Outline each blood parasite and name the species.
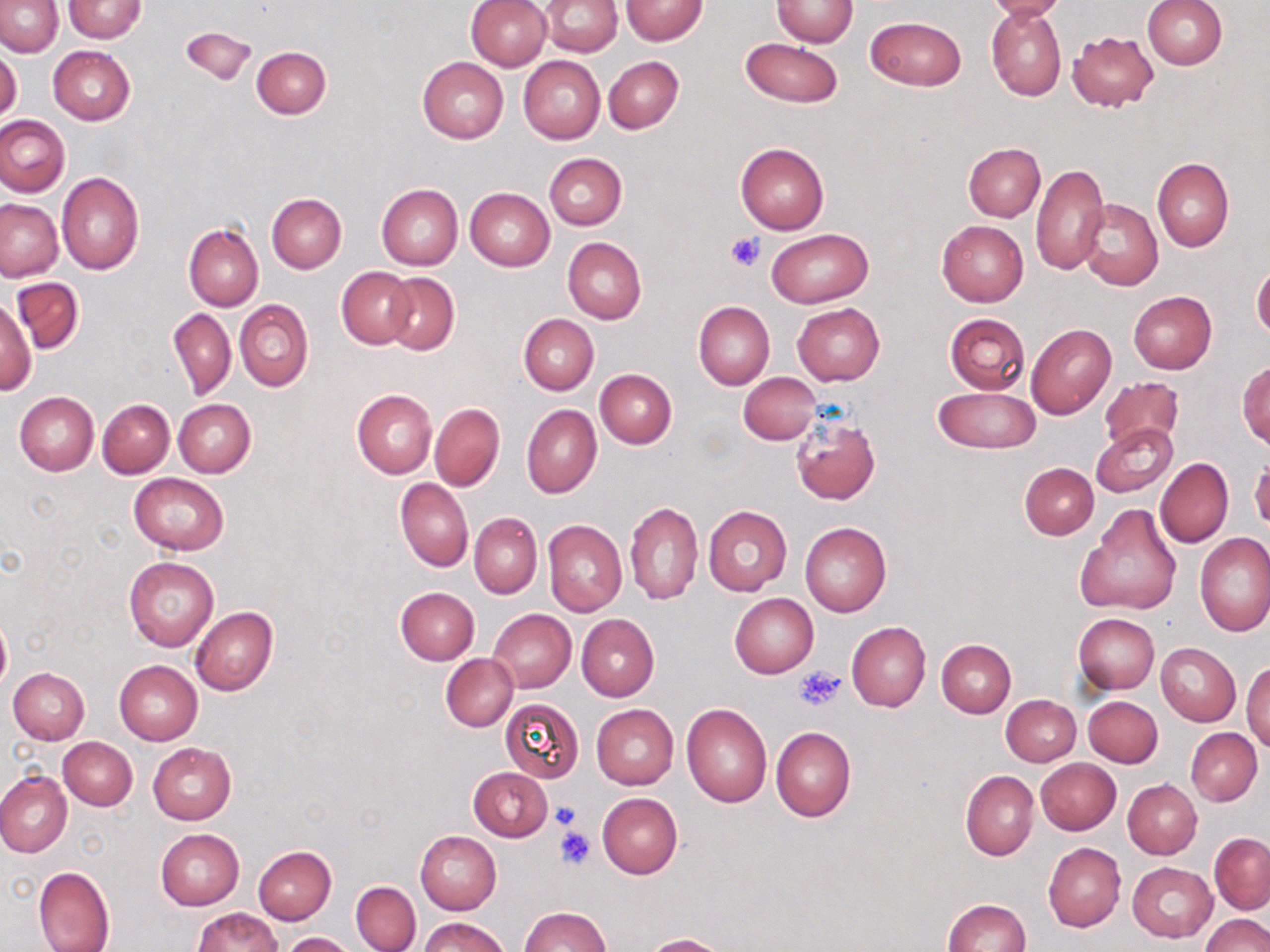
No blood parasites seen.

Summary:
  - Coordinate format: approximate bounding boxes as named x1/y1/x2/y2 corners in pixels
  - Platelet locations: (x1=726, y1=232, x2=766, y2=271), (x1=795, y1=666, x2=846, y2=711), (x1=552, y1=802, x2=582, y2=829), (x1=554, y1=825, x2=596, y2=869)
  - Uninfected red blood cell locations: (x1=0, y1=0, x2=64, y2=56), (x1=63, y1=0, x2=146, y2=43), (x1=540, y1=0, x2=622, y2=56), (x1=620, y1=0, x2=707, y2=45), (x1=771, y1=0, x2=858, y2=47), (x1=982, y1=0, x2=1067, y2=22), (x1=1142, y1=0, x2=1227, y2=68), (x1=467, y1=1, x2=552, y2=71), (x1=986, y1=6, x2=1066, y2=100), (x1=866, y1=15, x2=966, y2=90), (x1=181, y1=26, x2=257, y2=87), (x1=1068, y1=30, x2=1158, y2=112), (x1=741, y1=37, x2=843, y2=107), (x1=48, y1=46, x2=135, y2=125), (x1=0, y1=47, x2=23, y2=125), (x1=251, y1=47, x2=331, y2=119), (x1=518, y1=56, x2=605, y2=143), (x1=603, y1=56, x2=682, y2=133), (x1=418, y1=57, x2=508, y2=142), (x1=0, y1=115, x2=70, y2=197), (x1=735, y1=143, x2=829, y2=234), (x1=963, y1=143, x2=1044, y2=221), (x1=545, y1=153, x2=627, y2=229), (x1=1152, y1=158, x2=1234, y2=251), (x1=1031, y1=164, x2=1108, y2=275), (x1=56, y1=173, x2=144, y2=276), (x1=376, y1=184, x2=463, y2=270), (x1=465, y1=187, x2=555, y2=271), (x1=266, y1=193, x2=347, y2=273), (x1=1078, y1=198, x2=1162, y2=289), (x1=0, y1=200, x2=63, y2=281), (x1=937, y1=221, x2=1028, y2=306), (x1=184, y1=223, x2=263, y2=310), (x1=767, y1=229, x2=872, y2=306), (x1=563, y1=238, x2=647, y2=324), (x1=1251, y1=263, x2=1270, y2=340), (x1=337, y1=267, x2=416, y2=349), (x1=382, y1=273, x2=459, y2=355), (x1=12, y1=278, x2=84, y2=352), (x1=1128, y1=290, x2=1216, y2=374), (x1=0, y1=296, x2=35, y2=397), (x1=236, y1=300, x2=313, y2=391), (x1=693, y1=301, x2=774, y2=388), (x1=792, y1=303, x2=884, y2=385), (x1=168, y1=307, x2=236, y2=400), (x1=944, y1=312, x2=1030, y2=395), (x1=518, y1=313, x2=599, y2=394), (x1=1026, y1=323, x2=1116, y2=418), (x1=1237, y1=360, x2=1270, y2=449), (x1=595, y1=369, x2=676, y2=448), (x1=739, y1=372, x2=821, y2=444), (x1=1099, y1=375, x2=1186, y2=452), (x1=934, y1=386, x2=1040, y2=453), (x1=351, y1=390, x2=436, y2=478), (x1=14, y1=392, x2=99, y2=475), (x1=97, y1=399, x2=175, y2=478), (x1=173, y1=399, x2=256, y2=477), (x1=430, y1=403, x2=504, y2=491), (x1=521, y1=404, x2=601, y2=498), (x1=791, y1=415, x2=880, y2=504), (x1=1091, y1=422, x2=1177, y2=497), (x1=1155, y1=458, x2=1233, y2=548), (x1=1249, y1=459, x2=1270, y2=530), (x1=1019, y1=462, x2=1099, y2=540), (x1=129, y1=473, x2=229, y2=554), (x1=396, y1=478, x2=473, y2=572), (x1=624, y1=501, x2=703, y2=605), (x1=1078, y1=503, x2=1183, y2=616), (x1=703, y1=505, x2=792, y2=595), (x1=470, y1=513, x2=541, y2=599), (x1=543, y1=520, x2=626, y2=616), (x1=800, y1=522, x2=891, y2=617), (x1=1195, y1=533, x2=1270, y2=635), (x1=124, y1=556, x2=218, y2=651), (x1=395, y1=586, x2=480, y2=664), (x1=730, y1=593, x2=818, y2=677), (x1=190, y1=606, x2=277, y2=695), (x1=488, y1=609, x2=577, y2=692), (x1=1074, y1=613, x2=1159, y2=694), (x1=0, y1=614, x2=11, y2=693), (x1=577, y1=615, x2=658, y2=701), (x1=845, y1=622, x2=930, y2=710), (x1=936, y1=639, x2=1016, y2=718), (x1=1155, y1=642, x2=1241, y2=726), (x1=441, y1=654, x2=518, y2=730), (x1=114, y1=659, x2=203, y2=745), (x1=1242, y1=660, x2=1270, y2=751), (x1=8, y1=667, x2=89, y2=744), (x1=1001, y1=694, x2=1081, y2=766), (x1=1083, y1=696, x2=1162, y2=767), (x1=499, y1=698, x2=584, y2=783), (x1=681, y1=703, x2=772, y2=807), (x1=591, y1=704, x2=678, y2=789), (x1=771, y1=726, x2=856, y2=821), (x1=1185, y1=727, x2=1262, y2=805), (x1=59, y1=738, x2=137, y2=810), (x1=148, y1=743, x2=236, y2=824), (x1=1035, y1=758, x2=1121, y2=835), (x1=469, y1=768, x2=553, y2=841), (x1=960, y1=769, x2=1038, y2=861), (x1=0, y1=771, x2=72, y2=857), (x1=1123, y1=779, x2=1202, y2=858), (x1=597, y1=793, x2=683, y2=878), (x1=155, y1=828, x2=245, y2=909), (x1=415, y1=831, x2=502, y2=914), (x1=1210, y1=833, x2=1270, y2=913), (x1=1043, y1=843, x2=1125, y2=931), (x1=253, y1=845, x2=336, y2=923), (x1=1128, y1=861, x2=1216, y2=942), (x1=33, y1=865, x2=115, y2=952), (x1=350, y1=881, x2=421, y2=951), (x1=943, y1=899, x2=1031, y2=952), (x1=191, y1=906, x2=282, y2=951), (x1=519, y1=906, x2=611, y2=951), (x1=1200, y1=914, x2=1270, y2=952), (x1=420, y1=917, x2=509, y2=952), (x1=280, y1=932, x2=360, y2=952), (x1=642, y1=933, x2=733, y2=952)
  - Slide-level diagnosis: no evidence of blood parasites
  - Stain: May-Grünwald-Giemsa
  - Preparation: thin blood film
  - Image size: 1270×952 pixels
  - Magnification: 1000x
  - Modality: light microscopy
  - Field of view: single